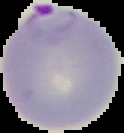

Summary:
  - Image type: segmented cell region on a black background
  - Result: malaria parasites detected
  - Preparation: thin blood film
  - Image size: 124×133 pixels